Draw a bounding box around every parasitised red blood cell.
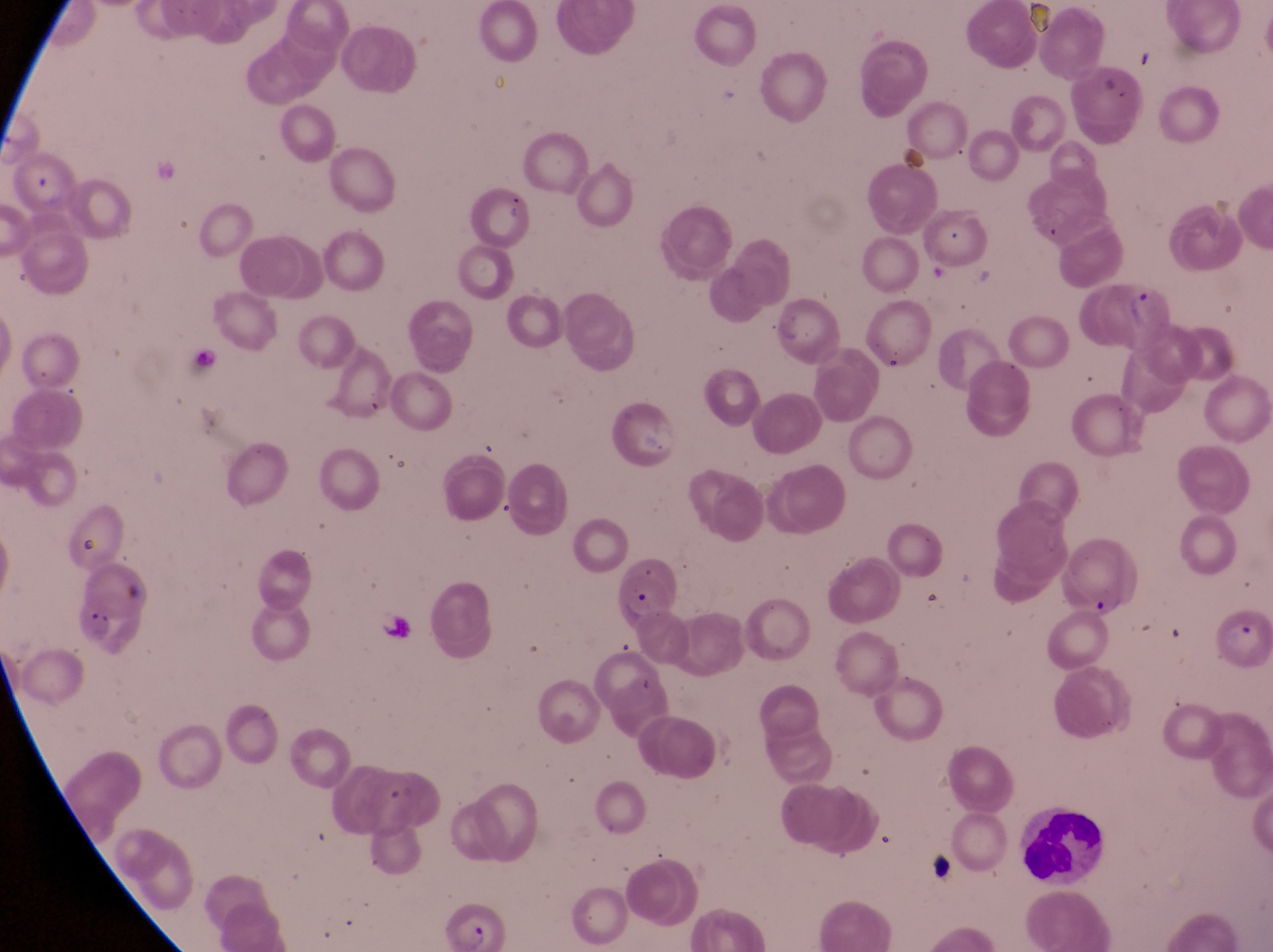

Approximate bounding boxes as [left, top, right, bottom] in pixels.
Parasitised red blood cells: [8, 152, 75, 210], [1099, 277, 1177, 354], [1064, 537, 1134, 622], [617, 569, 670, 631], [1210, 604, 1268, 664], [435, 899, 500, 952].

Leukocyte locations: [1011, 801, 1098, 888]. One field of view. Sample from Uganda. Captured by a smartphone held over the eyepiece of an Olympus CX-23 microscope. Image is 1273×952 pixels. Thin blood smear. At a magnification of 1000x.